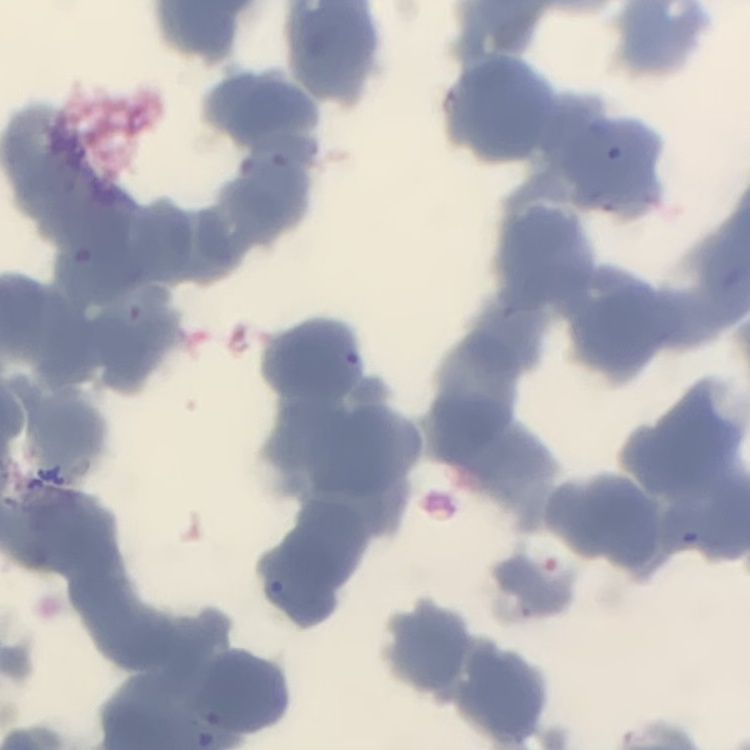

Summary:
  - Erythrocyte morphology: rouleaux formation
  - Image type: square crop of a larger photomicrograph
  - Preparation: thin peripheral smear
  - Stain: Field's or Giemsa